Name the cell type shown.
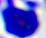
This is a leukocyte.

400x magnification. Micrograph.